Give the preparation type.
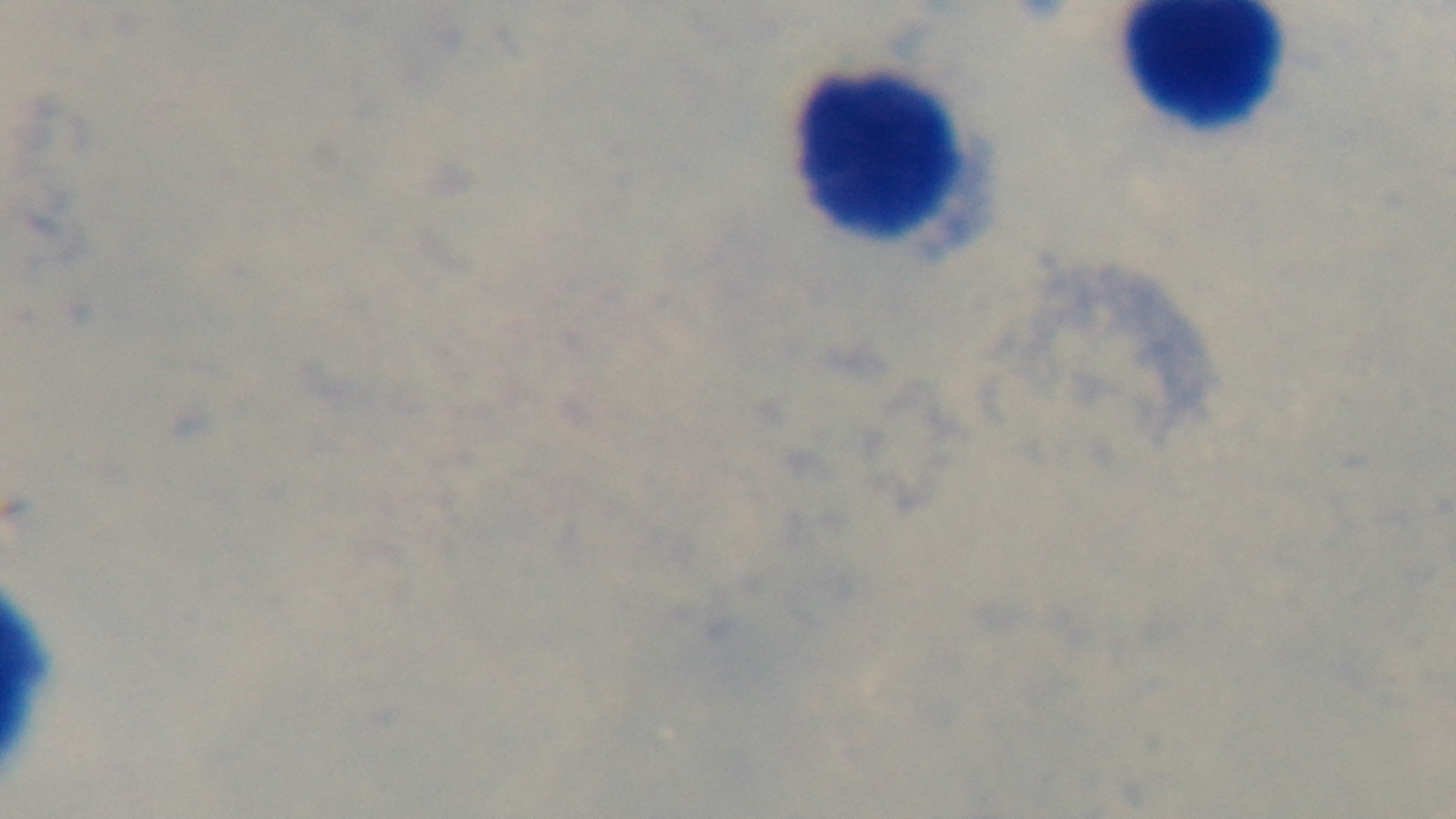

Thick.

Photomicrograph. Captured with a mounted 4K digital camera. One field from the slide. Giemsa stain. Malaria status: negative. 100x oil-immersion objective.